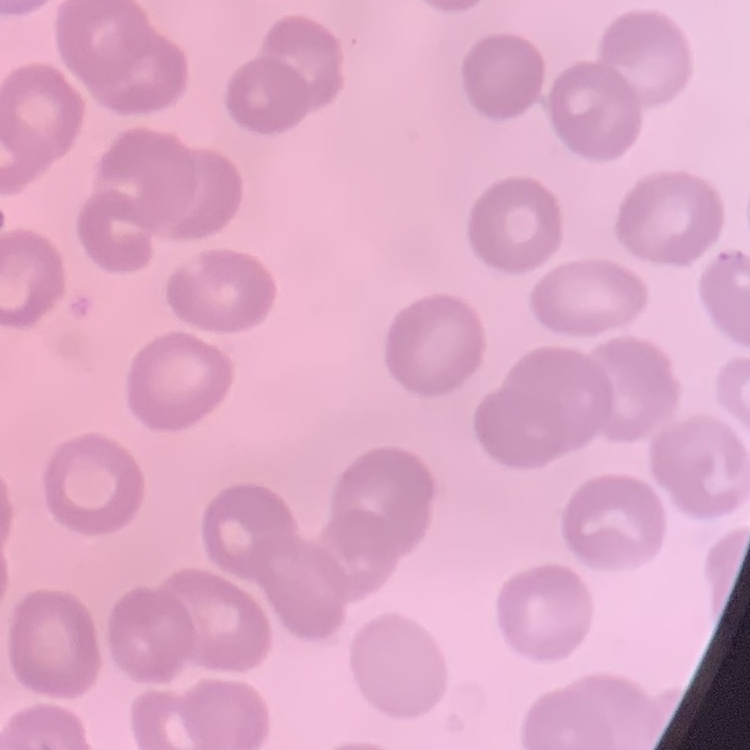
Summary:
  - Erythrocyte morphology: no rouleaux formation
  - Image type: one tile cut from a larger photomicrograph
  - Preparation: thin blood smear
  - Stain: Field's or Giemsa